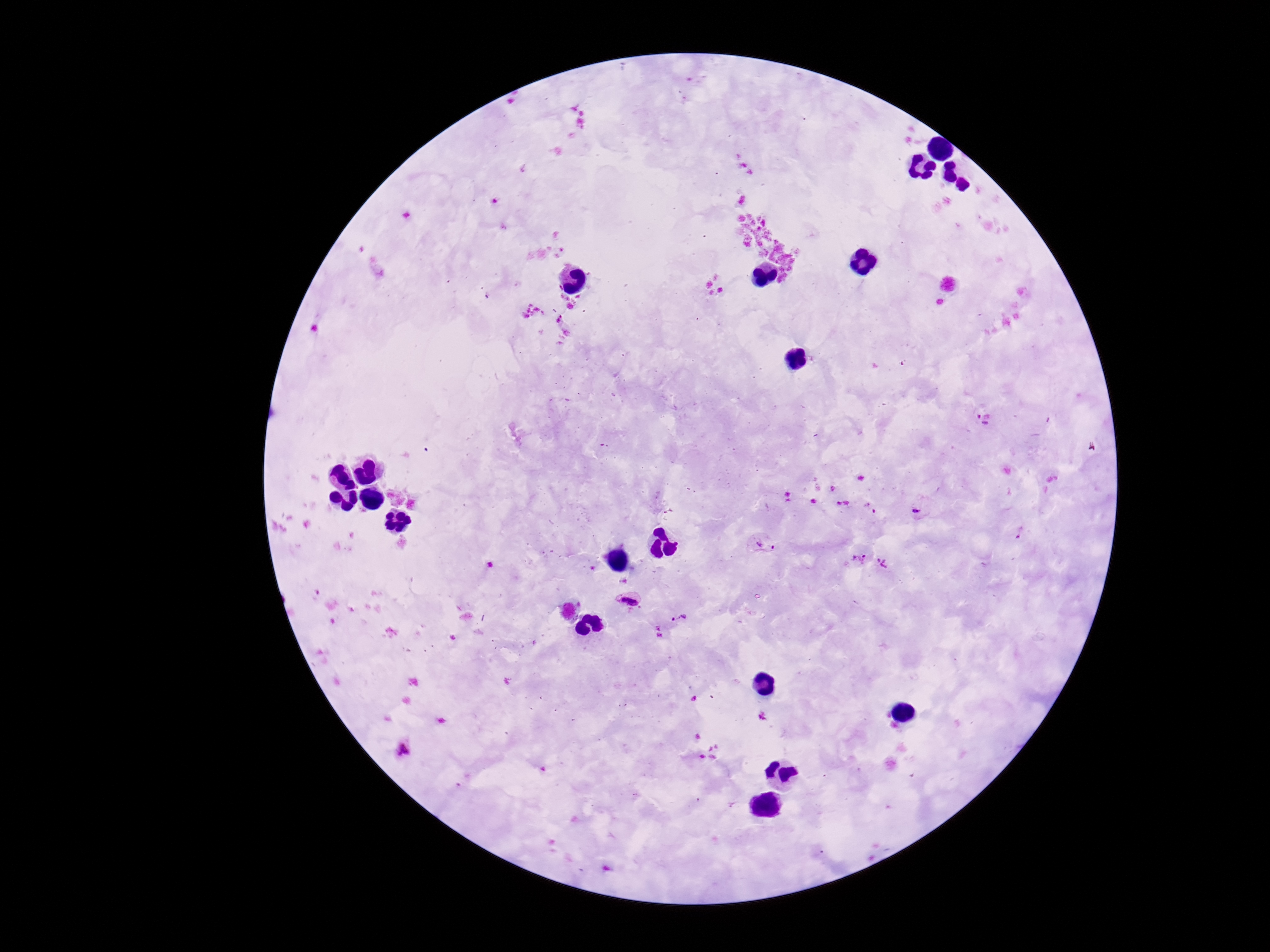 Approximate object centers, in pixels from the top-left corner. Plasmodium parasite locations: (x=984, y=417), (x=916, y=510), (x=1021, y=531), (x=763, y=545), (x=859, y=558), (x=882, y=564), (x=629, y=598), (x=679, y=618). Patient malaria status: infected. Giemsa stain. Image is 1270×952 pixels. Photographed through the microscope eyepiece with a smartphone camera. 100x magnification. Single field of view. Thick peripheral-blood smear.